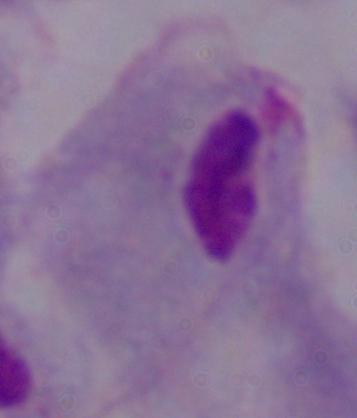 1000x magnification. Photomicrograph. A trichomonad is shown.